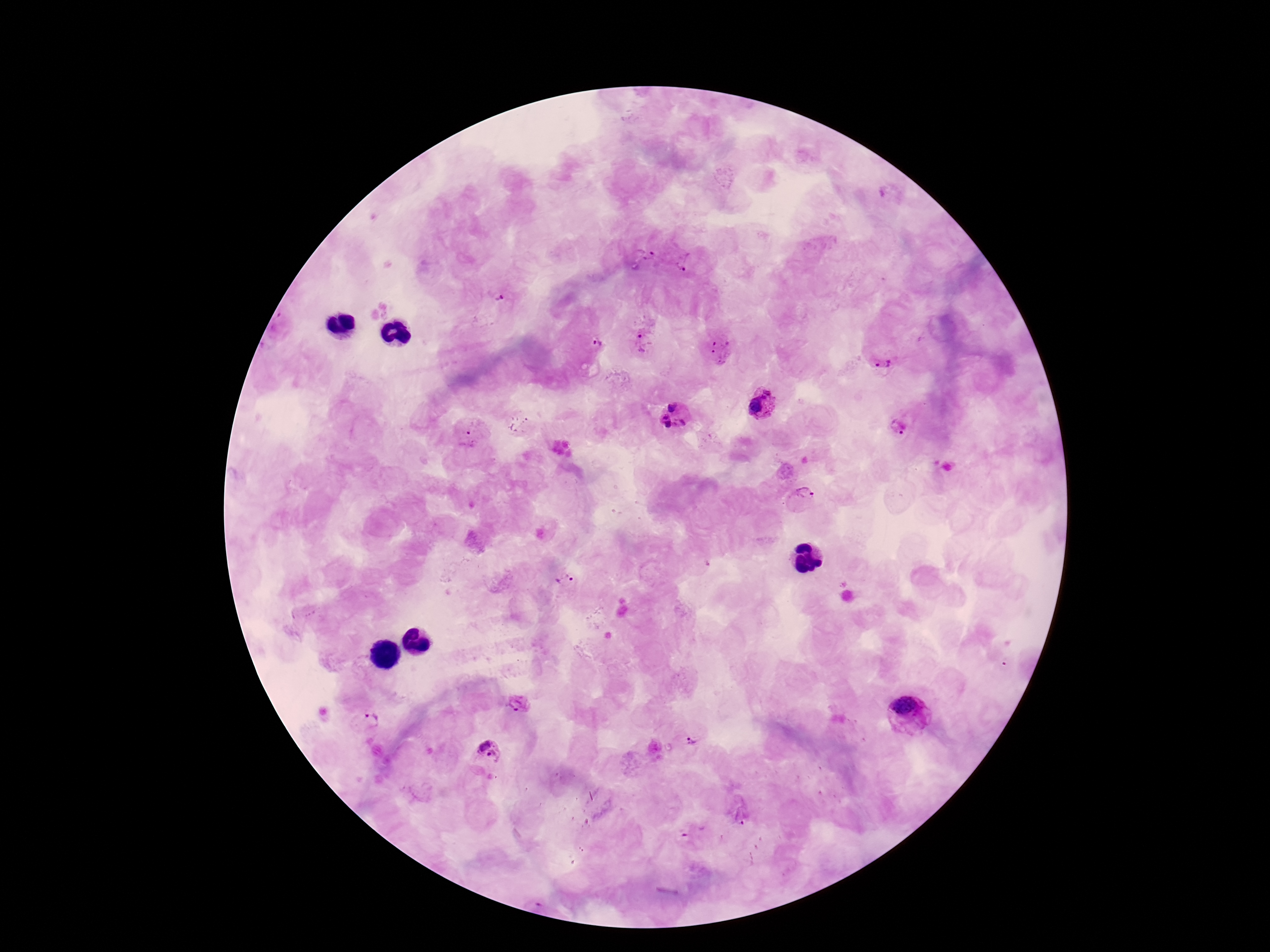
Approximate centers as {x, y} in pixels. Plasmodium parasite locations: {646, 257}, {688, 262}, {498, 293}, {643, 340}, {590, 345}, {721, 350}, {881, 352}, {763, 405}, {674, 415}, {520, 423}, {902, 425}, {470, 433}, {805, 498}, {567, 579}, {519, 703}, {908, 715}, {367, 720}, {692, 740}, {489, 752}, {740, 810}. Patient malaria status: infected. 100x magnification. One field from this slide. Image is 1270×952 pixels. Thick blood smear. Smartphone photograph taken through the microscope eyepiece. Giemsa-stained preparation.